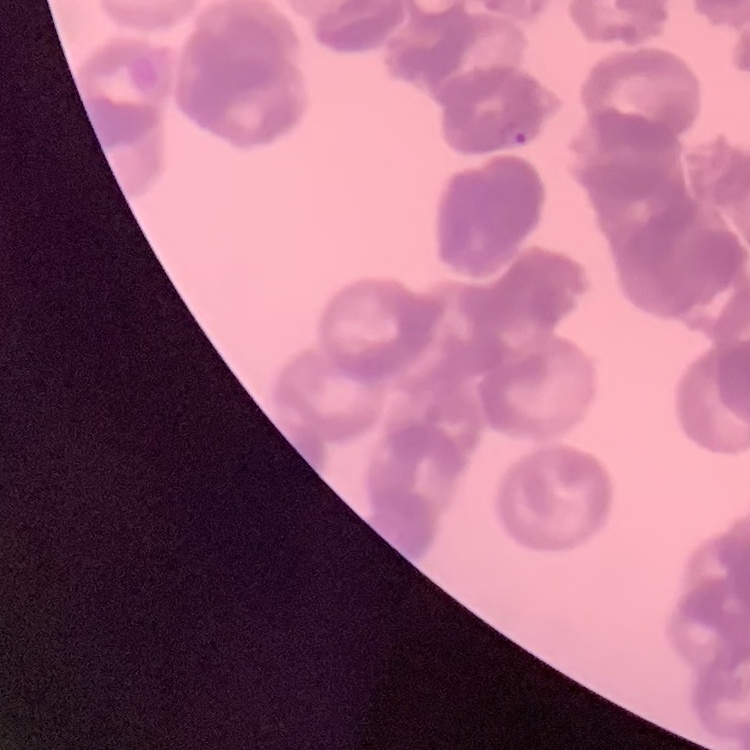

The red blood cells exhibit rouleaux formation. Field's or Giemsa stain. One tile cut from a larger photomicrograph. Thin blood smear.